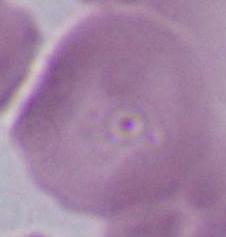
modality = photomicrograph
magnification = 1000x
identification = erythrocyte